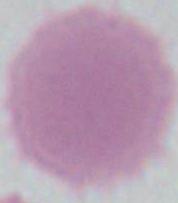
modality = micrograph
magnification = 1000x
identification = erythrocyte